Classify this cell by malaria status.
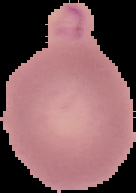
It is uninfected.

Cell region segmented out of the field of view; the surrounding area is masked to black. Image is 136×193 pixels. From a thin blood smear.